Give the position of every leukocyte visible.
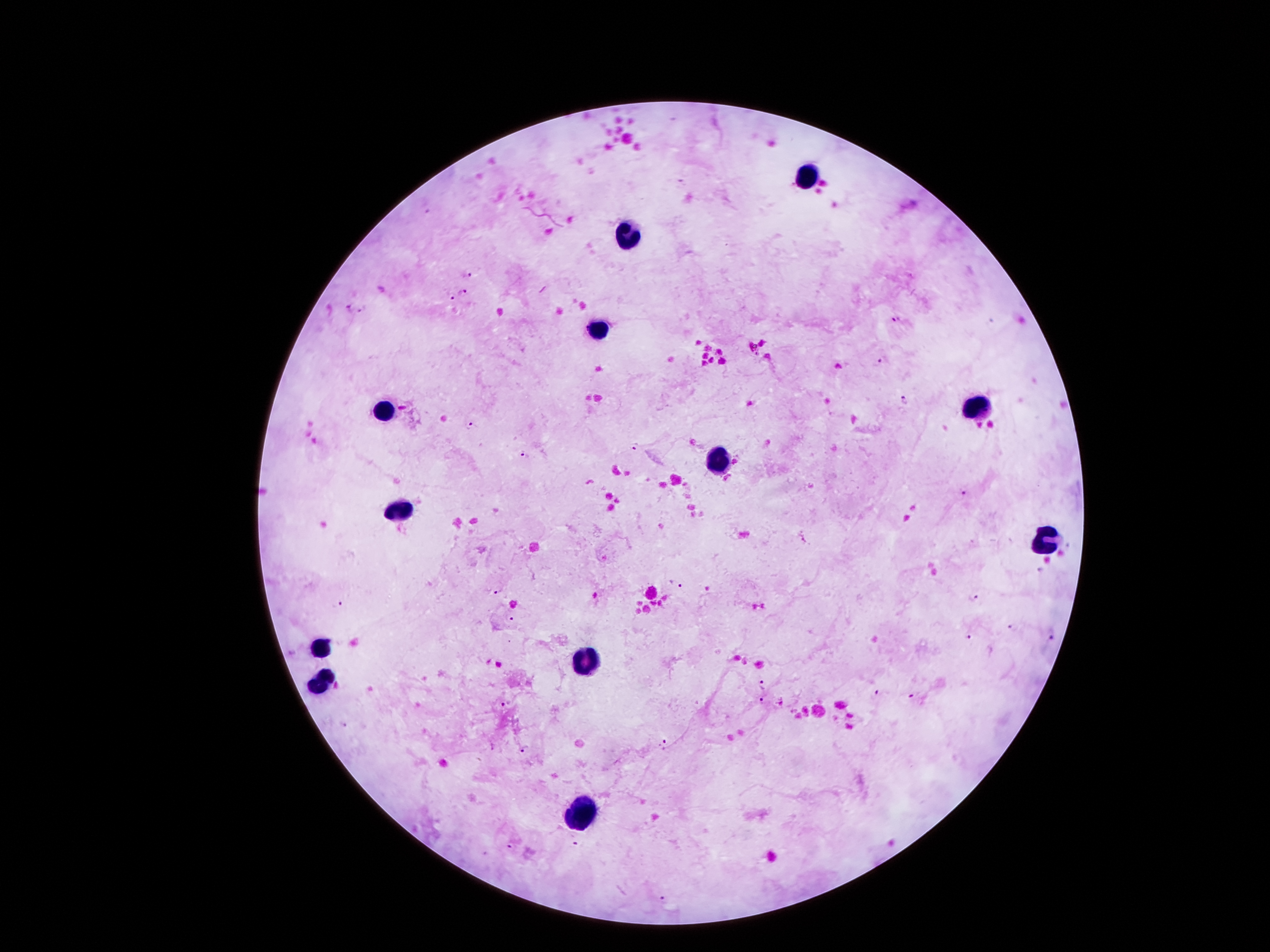
Approximate centers as (x, y) in pixels.
Leukocytes: (809, 174), (629, 236), (599, 330), (977, 404), (386, 410), (716, 458), (402, 510), (1044, 539), (323, 650), (587, 663), (323, 683), (584, 815).

Plasmodium parasite locations: (465, 272), (464, 293), (454, 297), (349, 306), (362, 312), (897, 317), (882, 361), (904, 400), (470, 425), (635, 445), (524, 454), (965, 494), (674, 584), (496, 590), (971, 597), (338, 604), (513, 619), (1015, 629), (967, 636), (1052, 636), (763, 683), (877, 692), (911, 695), (764, 701), (505, 704), (665, 745), (522, 747), (578, 845), (511, 847), (663, 899). Single field of view. Patient malaria status: infected with Plasmodium falciparum. Thick peripheral-blood smear. Image is 1270×952 pixels. Giemsa stain. 100x magnification. Photographed through the microscope eyepiece with a smartphone camera.